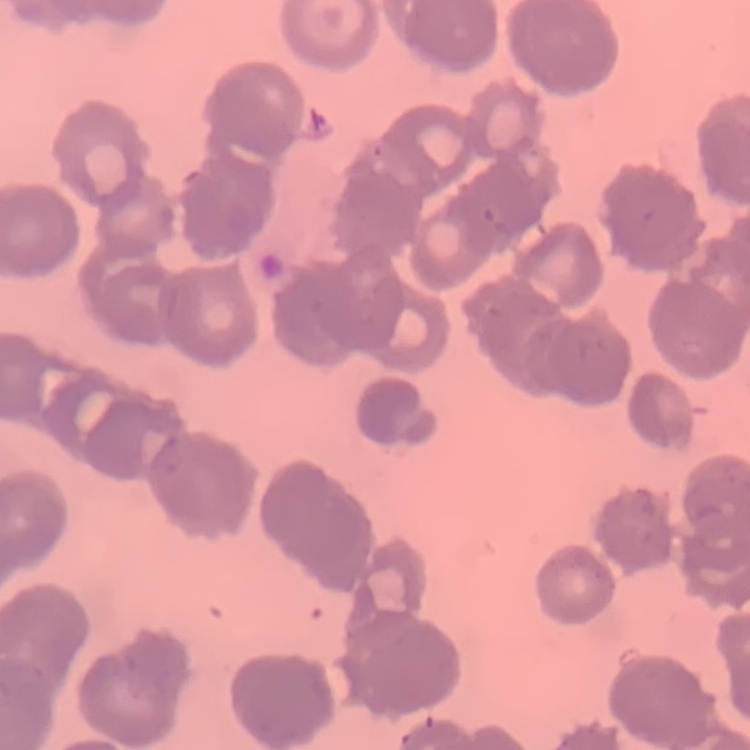

Summary:
  - Erythrocyte morphology: rouleaux formation
  - Stain: Field's or Giemsa
  - Image type: square crop of a larger photomicrograph
  - Preparation: thin blood smear